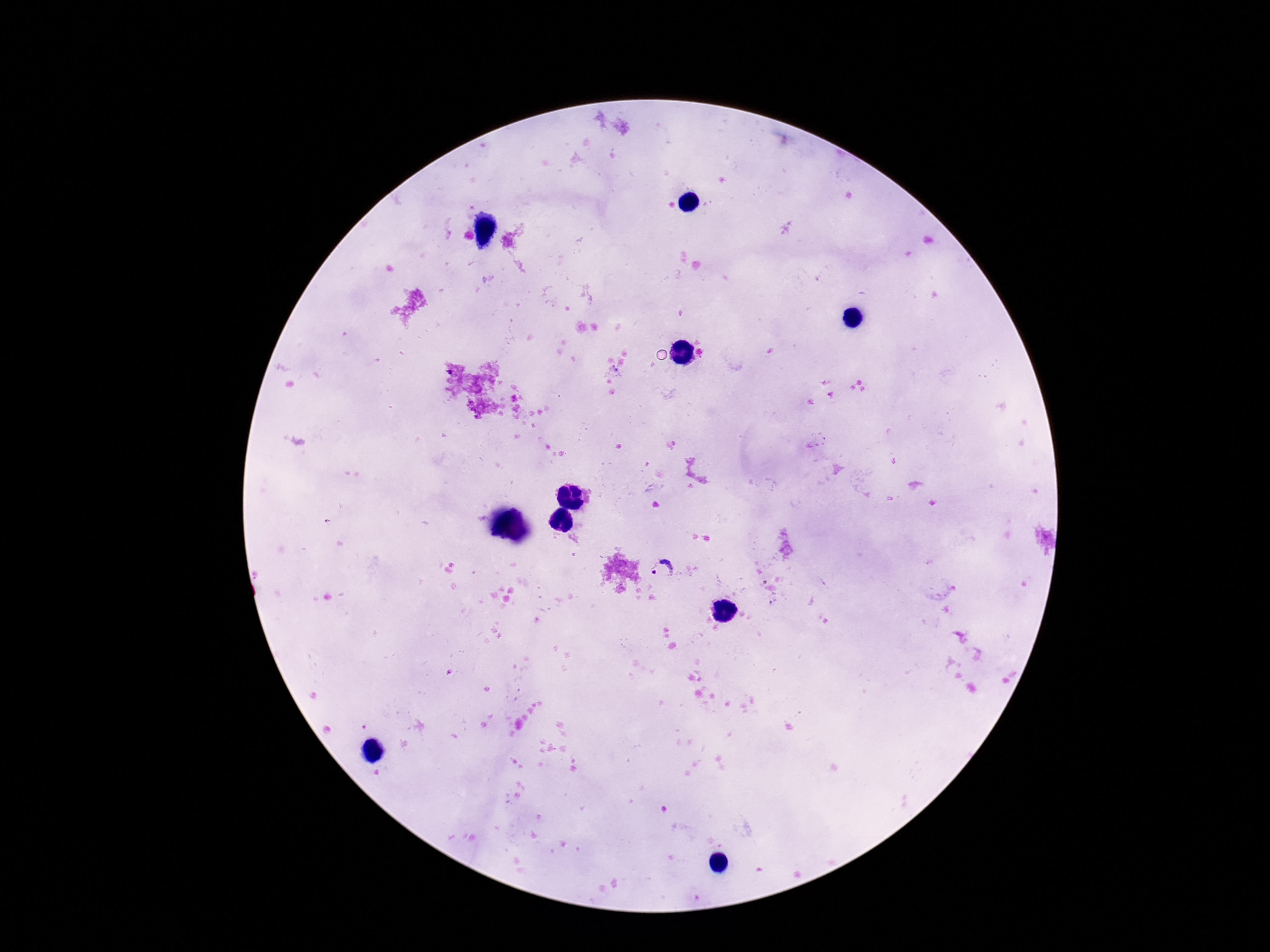

Approximate centers as {x, y} in pixels. Plasmodium parasite locations: {664, 571}. Smartphone photograph taken through the microscope eyepiece. Image is 1270×952 pixels. Single field of view. Patient malaria status: positive. Thick blood smear. Giemsa stain. 100x magnification.